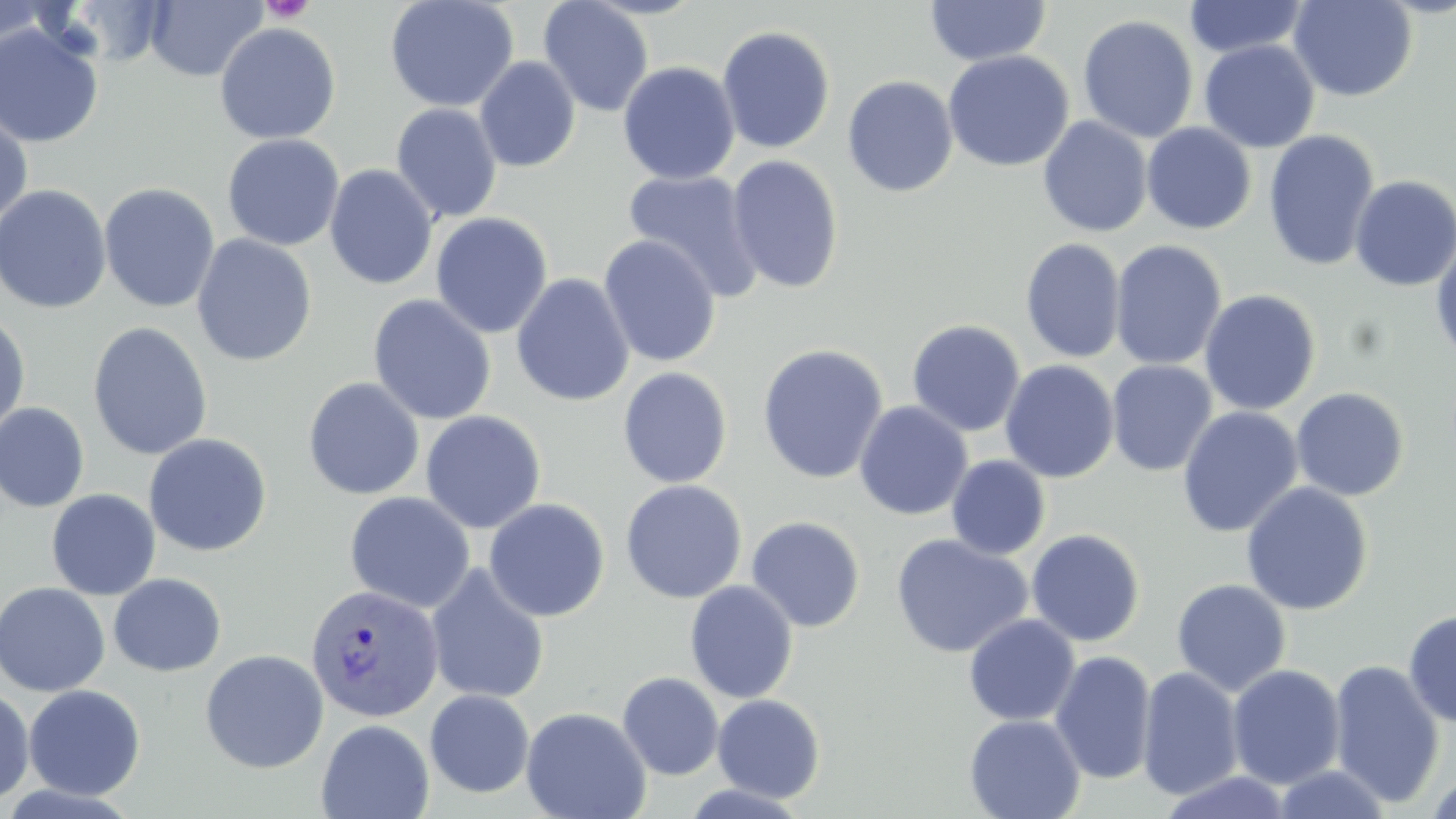
slide-level diagnosis = Plasmodium vivax
platelet locations = approximate bounding boxes as [x1, y1, x2, y2] in pixels: [259, 0, 315, 24]
Plasmodium vivax-infected red blood cell locations = approximate bounding boxes as [x1, y1, x2, y2] in pixels: [305, 583, 444, 723]
stain = May-Grünwald-Giemsa
image size = 1456×819 pixels
uninfected red blood cell locations = approximate bounding boxes as [x1, y1, x2, y2] in pixels: [1, 0, 60, 55], [384, 0, 519, 113], [537, 0, 654, 118], [1288, 0, 1418, 102], [145, 1, 268, 83], [923, 1, 1053, 67], [1182, 1, 1311, 59], [1078, 14, 1198, 143], [0, 22, 104, 148], [214, 22, 341, 145], [716, 25, 836, 155], [1198, 40, 1320, 153], [942, 50, 1074, 172], [474, 56, 581, 172], [617, 61, 739, 185], [842, 75, 959, 197], [390, 103, 503, 224], [0, 106, 34, 232], [1038, 116, 1153, 238], [1141, 123, 1257, 234], [1263, 129, 1381, 272], [222, 133, 344, 251], [726, 154, 845, 294], [323, 164, 438, 291], [622, 169, 765, 302], [1349, 174, 1456, 291], [98, 182, 220, 313], [0, 184, 112, 314], [430, 212, 553, 339], [191, 234, 317, 367], [598, 234, 722, 368], [1020, 238, 1125, 364], [1110, 239, 1227, 371], [1431, 239, 1456, 366], [511, 272, 634, 407], [1199, 289, 1321, 416], [368, 294, 497, 425], [0, 312, 31, 437], [906, 319, 1026, 437], [87, 321, 213, 460], [757, 343, 889, 485], [1000, 359, 1120, 483], [1106, 360, 1218, 477], [618, 367, 733, 488], [302, 377, 425, 500], [1290, 387, 1410, 501], [853, 400, 974, 520], [0, 403, 90, 513], [1176, 406, 1303, 538], [420, 410, 547, 533], [143, 433, 272, 556], [946, 455, 1051, 560], [620, 479, 747, 604], [1240, 481, 1374, 616], [46, 489, 161, 600], [344, 491, 475, 613], [483, 498, 610, 622], [746, 515, 866, 632], [1026, 529, 1146, 646], [891, 533, 1033, 658], [425, 563, 550, 704], [108, 573, 226, 676], [1171, 579, 1292, 696], [684, 580, 799, 703], [0, 581, 110, 697], [1403, 609, 1456, 727], [963, 614, 1081, 727], [199, 649, 329, 773], [1049, 650, 1157, 784], [1328, 660, 1445, 807], [1227, 663, 1346, 787], [1137, 666, 1244, 799], [617, 672, 724, 780], [23, 684, 146, 800], [0, 687, 34, 806], [424, 689, 535, 798], [712, 693, 826, 802], [520, 706, 651, 819], [963, 713, 1086, 819], [316, 718, 434, 819], [1269, 763, 1394, 818], [1424, 770, 1456, 819], [1156, 771, 1295, 819], [679, 783, 812, 818]
magnification = 1000x
preparation = thin blood film
modality = light microscopy
field of view = one of a larger specimen